Assess this cell for malaria.
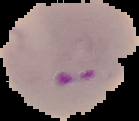
Parasitized.

Summary:
  - Preparation: thin blood film
  - Image size: 139×121 pixels
  - Image type: cell region segmented out of the field of view; surrounding area masked to black